Locate every uninfected red blood cell.
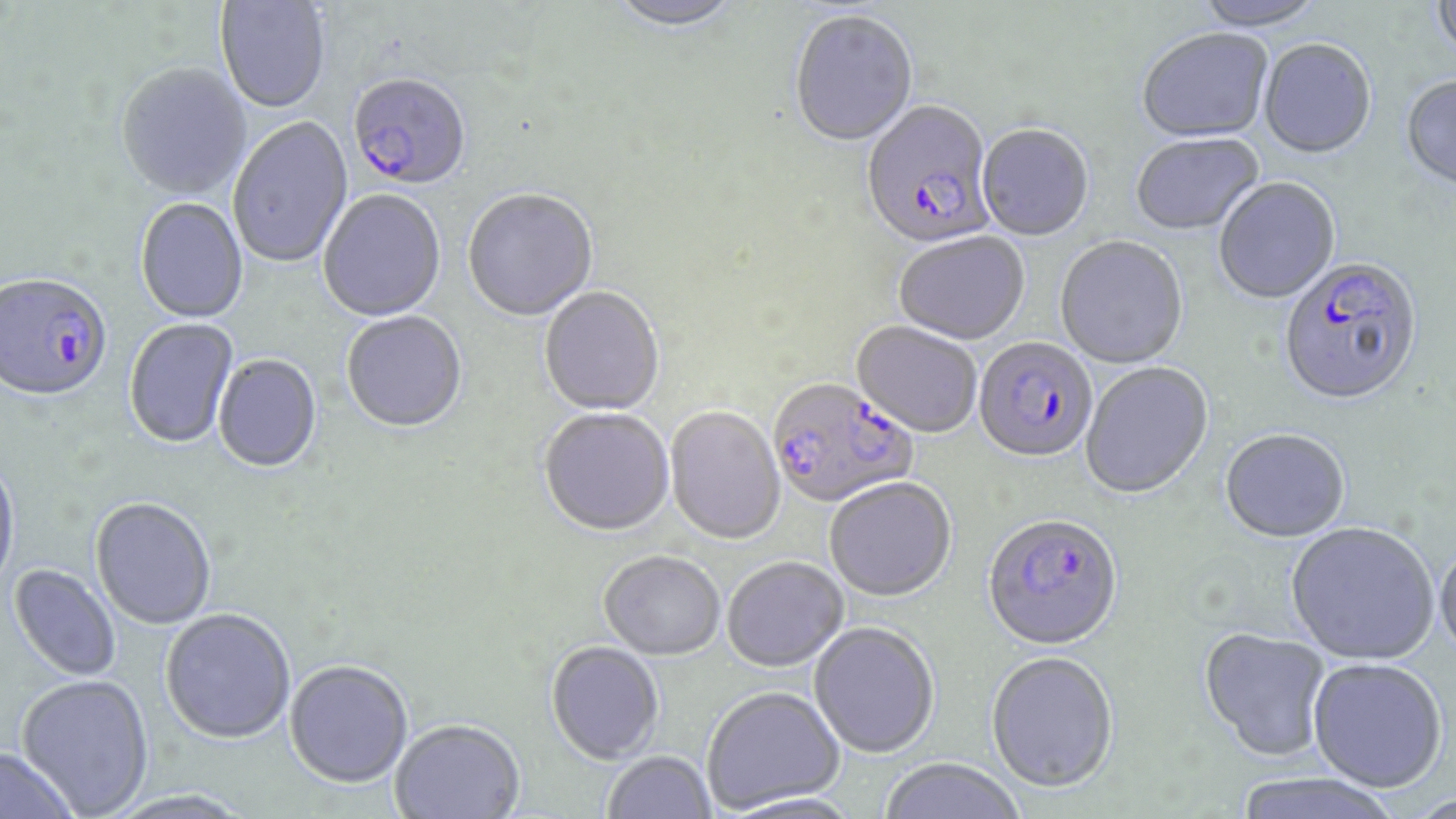

Approximate bounding boxes as (x1, y1, x2, y2) in pixels.
Uninfected red blood cells: (606, 0, 745, 35), (1431, 0, 1456, 65), (215, 1, 331, 115), (1193, 1, 1329, 31), (789, 12, 919, 150), (1136, 30, 1274, 145), (1259, 41, 1376, 161), (116, 65, 252, 201), (1400, 77, 1456, 197), (228, 118, 354, 270), (977, 126, 1094, 243), (1131, 135, 1265, 238), (1213, 179, 1340, 306), (318, 190, 446, 323), (463, 190, 598, 324), (135, 199, 249, 324), (893, 233, 1028, 346), (1055, 238, 1188, 371), (539, 288, 665, 417), (342, 313, 467, 435), (124, 318, 240, 450), (851, 322, 981, 439), (213, 355, 322, 474), (1080, 362, 1214, 501), (665, 407, 785, 546), (538, 410, 675, 539), (1219, 430, 1350, 544), (0, 457, 20, 595), (825, 479, 956, 604), (90, 499, 216, 631), (1285, 523, 1439, 667), (1434, 542, 1456, 666), (598, 554, 725, 662), (722, 559, 848, 674), (8, 564, 120, 681), (160, 611, 296, 746), (809, 623, 939, 759), (1198, 629, 1332, 763), (545, 643, 664, 766), (986, 653, 1119, 794), (1308, 661, 1447, 795), (284, 662, 413, 791), (16, 675, 154, 817), (703, 688, 844, 815), (390, 721, 525, 819), (0, 747, 79, 819), (602, 752, 715, 818), (878, 758, 1027, 819), (1231, 774, 1404, 819), (107, 790, 254, 819), (1405, 795, 1456, 819).

slide_level_diagnosis: Plasmodium falciparum
image_size: 1456×819 pixels
plasmodium_falciparum_infected_red_blood_cell_locations: 'approximate bounding boxes as (x1, y1, x2, y2) in pixels: (353, 77, 468, 191), (861, 102, 999, 253), (1278, 259, 1423, 408), (0, 276, 113, 404), (974, 338, 1097, 465), (767, 380, 918, 511), (982, 516, 1122, 653)'
magnification: 1000x
stain: May-Grünwald-Giemsa
modality: light microscopy
preparation: thin blood film
field_of_view: one of a larger specimen